Locate every blood parasite and identify its species.
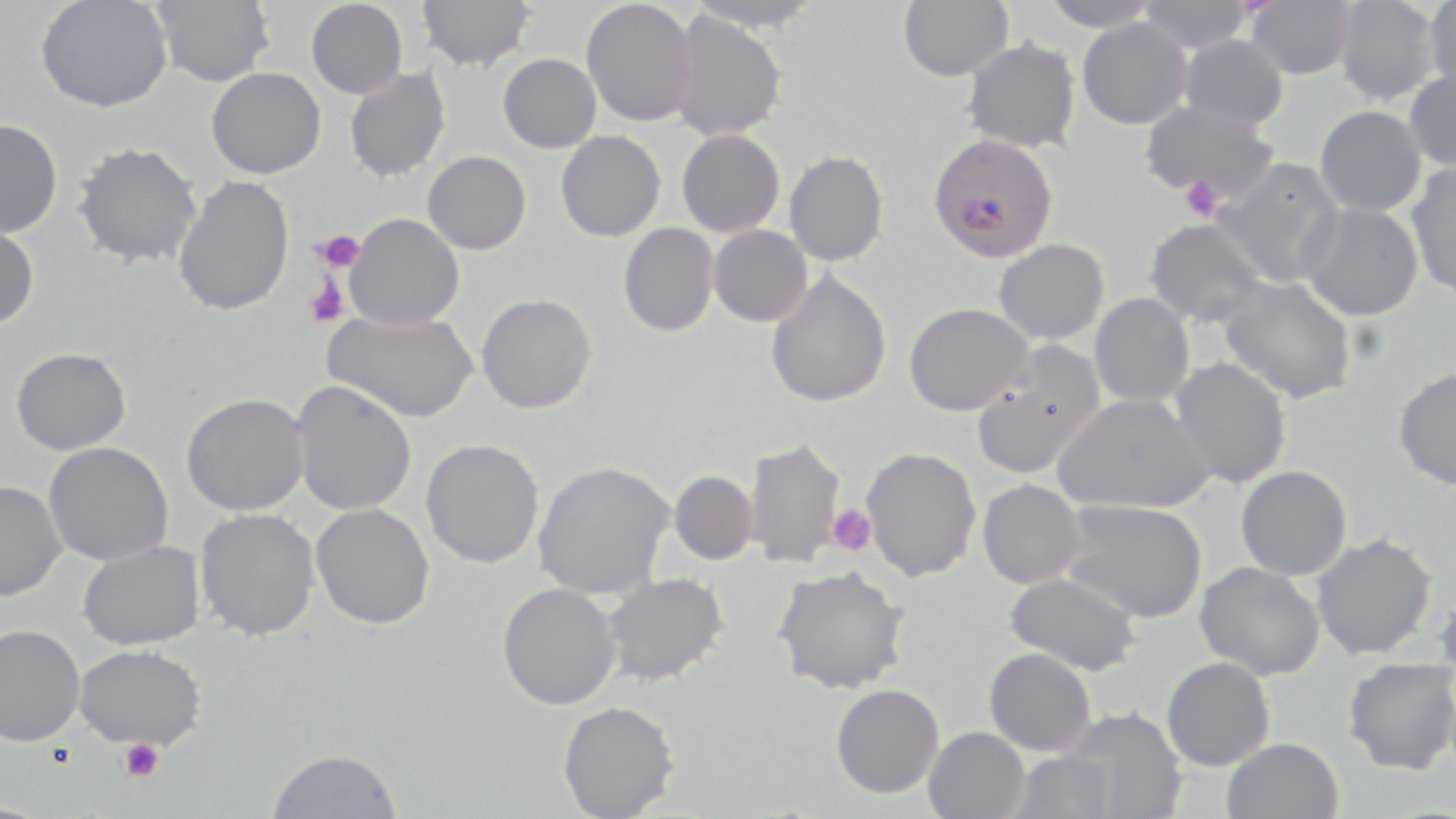
Approximate bounding boxes as (x1, y1, x2, y2) in pixels.
Plasmodium falciparum-infected red blood cells: (928, 133, 1059, 262).
No Plasmodium ovale, Plasmodium malariae, Plasmodium vivax, Babesia divergens, or Trypanosoma brucei observed.

Summary:
  - Uninfected red blood cell locations: (36, 0, 172, 113), (152, 0, 275, 87), (306, 0, 408, 98), (417, 0, 535, 72), (581, 0, 697, 126), (898, 0, 1013, 81), (1039, 0, 1161, 31), (1138, 0, 1253, 53), (1333, 0, 1442, 105), (1423, 0, 1456, 93), (684, 1, 824, 31), (1246, 1, 1355, 79), (669, 10, 787, 141), (1077, 18, 1192, 129), (1179, 35, 1288, 131), (962, 37, 1080, 153), (498, 53, 601, 153), (206, 67, 326, 179), (344, 67, 450, 182), (1404, 68, 1456, 171), (1139, 101, 1279, 204), (1314, 105, 1426, 217), (0, 119, 62, 237), (677, 129, 785, 237), (555, 130, 665, 241), (72, 140, 201, 268), (784, 150, 889, 266), (422, 151, 531, 254), (1213, 158, 1346, 287), (1406, 160, 1456, 300), (173, 175, 294, 316), (1300, 203, 1424, 321), (344, 214, 464, 330), (1144, 218, 1268, 327), (0, 222, 39, 330), (618, 223, 719, 337), (709, 225, 813, 327), (993, 238, 1110, 345), (766, 271, 892, 408), (1218, 276, 1357, 404), (477, 293, 597, 413), (1089, 293, 1195, 407), (904, 302, 1033, 415), (323, 309, 477, 422), (970, 342, 1106, 479), (11, 347, 131, 454), (1169, 357, 1293, 489), (1392, 366, 1456, 491), (290, 380, 417, 515), (181, 393, 308, 516), (1053, 393, 1213, 514), (743, 436, 847, 568), (421, 438, 544, 568), (42, 441, 174, 565), (859, 447, 981, 581), (533, 460, 675, 599), (1235, 465, 1352, 580), (669, 470, 758, 565), (977, 479, 1086, 589), (0, 480, 65, 601), (1060, 499, 1207, 623), (311, 503, 434, 629), (195, 508, 320, 641), (1310, 533, 1438, 659), (77, 541, 205, 650), (1195, 561, 1325, 680), (772, 565, 910, 695), (1004, 571, 1143, 675), (602, 572, 729, 686), (497, 583, 621, 709), (1432, 585, 1456, 672), (0, 624, 85, 745), (73, 644, 206, 750), (984, 647, 1097, 756), (1161, 656, 1275, 771), (1343, 658, 1456, 774), (831, 684, 944, 799), (557, 701, 680, 819), (1059, 705, 1187, 818), (923, 726, 1030, 819), (1221, 737, 1343, 819), (267, 748, 402, 819), (1006, 750, 1116, 819)
  - Platelet locations: (1178, 176, 1224, 222), (313, 230, 364, 273), (305, 278, 349, 329), (827, 504, 876, 555), (119, 739, 164, 783)
  - Slide-level diagnosis: Plasmodium falciparum
  - Image size: 1456×819 pixels
  - Modality: optical microscopy
  - Stain: May-Grünwald-Giemsa
  - Field of view: one of a larger specimen
  - Magnification: 1000x
  - Preparation: thin blood film